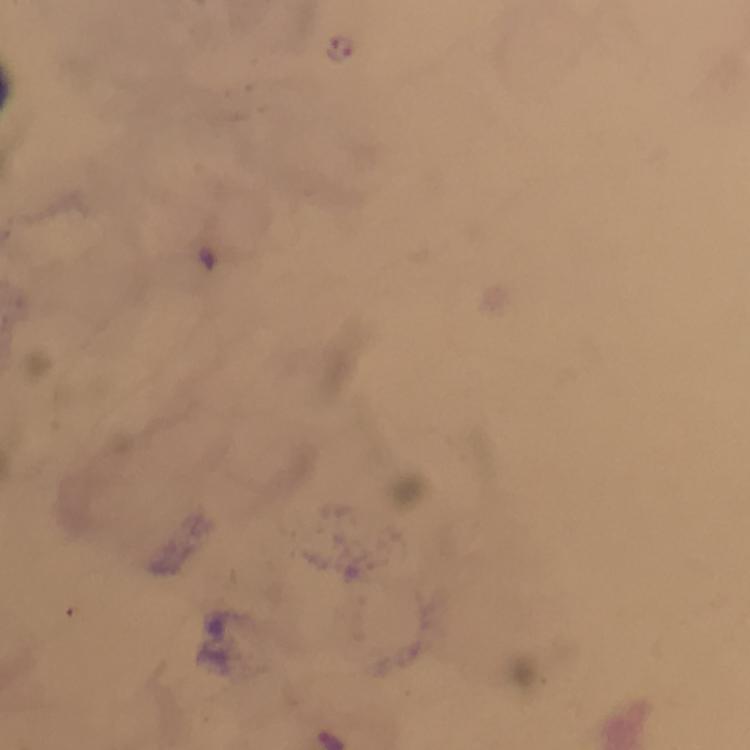

{
  "immersion_oil": "used",
  "context": "from a malaria diagnostic workup",
  "stain": "Giemsa",
  "preparation": "thick blood film",
  "capture": "smartphone mounted on the microscope",
  "cropped_from": "one field of view",
  "magnification": "100x",
  "plasmodium_parasite_locations": "approximate centers as {x, y} in pixels: {341, 47}",
  "image_size": "750×750 pixels"
}